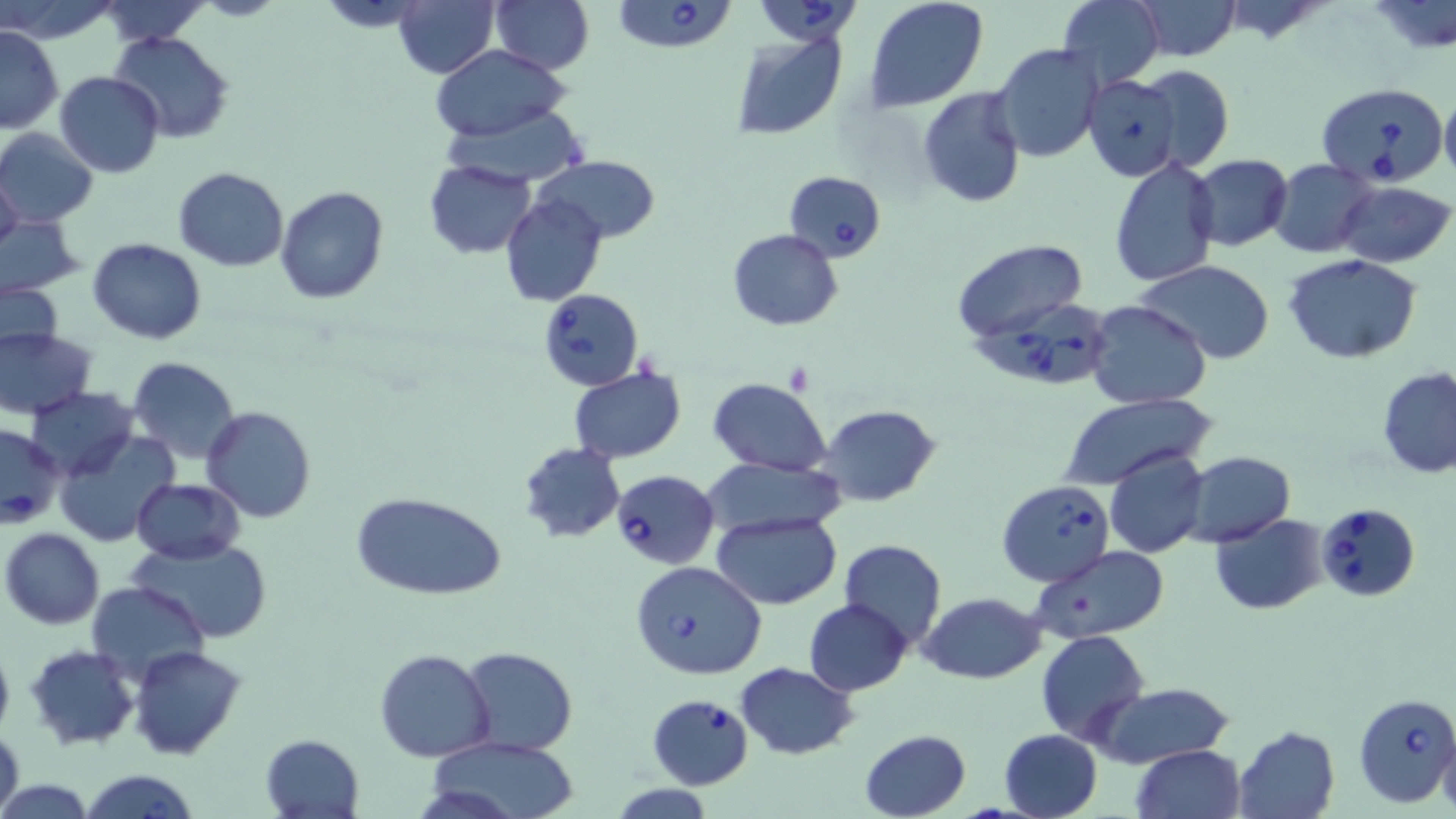

Approximate bounding boxes as (x1, y1, x2, y2) in pixels. Uninfected red blood cell locations: (0, 0, 120, 43), (96, 0, 209, 47), (321, 0, 426, 31), (475, 0, 592, 146), (489, 0, 593, 74), (865, 0, 989, 114), (1056, 0, 1165, 89), (1131, 0, 1240, 60), (1369, 0, 1455, 55), (394, 1, 498, 77), (0, 26, 64, 133), (109, 31, 234, 145), (731, 31, 848, 139), (993, 42, 1105, 164), (430, 44, 571, 143), (1131, 64, 1234, 175), (55, 71, 164, 176), (1078, 72, 1186, 183), (1440, 86, 1456, 191), (916, 87, 1026, 207), (439, 100, 587, 187), (0, 128, 99, 228), (1109, 154, 1220, 288), (1189, 154, 1292, 251), (535, 155, 659, 243), (423, 159, 537, 258), (1268, 159, 1379, 257), (0, 165, 24, 258), (173, 166, 289, 272), (1335, 181, 1454, 266), (275, 184, 388, 305), (501, 193, 605, 307), (1, 217, 85, 295), (727, 228, 843, 331), (88, 238, 206, 344), (953, 240, 1089, 344), (1284, 253, 1424, 363), (1132, 261, 1278, 364), (2, 282, 65, 353), (1085, 301, 1213, 412), (0, 328, 96, 419), (127, 357, 243, 463), (568, 366, 688, 464), (1377, 366, 1456, 477), (708, 378, 832, 475), (26, 387, 139, 479), (1057, 393, 1213, 492), (819, 404, 940, 507), (201, 406, 315, 524), (52, 430, 178, 546), (517, 442, 626, 544), (1104, 448, 1210, 561), (1181, 450, 1295, 547), (703, 457, 848, 537), (133, 478, 245, 563), (353, 491, 505, 602), (711, 511, 841, 609), (1209, 513, 1328, 615), (2, 527, 104, 629), (128, 538, 272, 644), (838, 539, 946, 647), (1032, 546, 1171, 643), (86, 580, 210, 686), (921, 592, 1044, 684), (804, 600, 911, 696), (1036, 630, 1149, 745), (0, 640, 15, 740), (24, 643, 140, 750), (130, 646, 247, 761), (374, 647, 496, 763), (460, 647, 578, 753), (734, 662, 858, 759), (1090, 683, 1236, 768), (0, 724, 24, 819), (1234, 725, 1340, 818), (860, 728, 971, 819), (999, 729, 1103, 819), (1438, 729, 1456, 819), (259, 733, 364, 817), (426, 736, 580, 819), (1130, 744, 1245, 819), (80, 768, 198, 819). Babesia divergens-infected red blood cell locations: (751, 0, 862, 46), (611, 1, 740, 53), (1316, 81, 1448, 187), (784, 170, 886, 262), (537, 288, 644, 391), (977, 297, 1118, 391), (1, 424, 67, 528), (610, 469, 721, 569), (996, 479, 1114, 587), (1317, 502, 1420, 600), (629, 560, 768, 680), (648, 693, 755, 790), (1354, 693, 1456, 808). Slide-level diagnosis: Babesia divergens. Thin blood film. 1000x magnification. Image is 1456×819 pixels. Light microscopy. May-Grünwald-Giemsa stain. Single field of view.